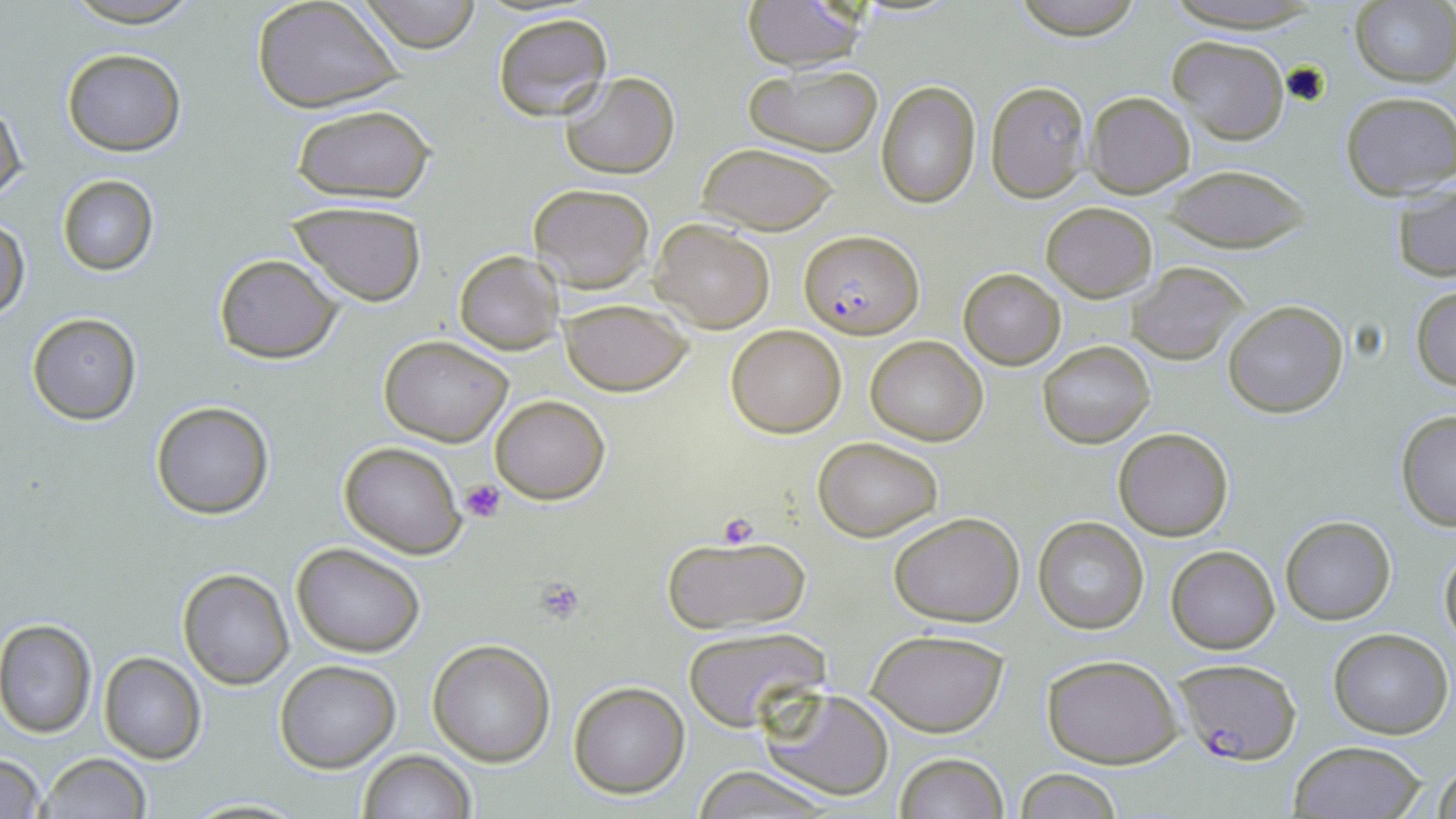

slide_level_diagnosis: Plasmodium falciparum
stain: May-Grünwald-Giemsa
field_of_view: single
preparation: thin blood smear
uninfected_red_blood_cell_locations: 'approximate bounding boxes as [x1, y1, x2, y2] in pixels: [57, 0, 209, 26], [252, 0, 405, 114], [356, 0, 485, 53], [1008, 0, 1147, 41], [1159, 0, 1323, 33], [741, 1, 869, 70], [1351, 3, 1456, 85], [491, 12, 613, 122], [1165, 35, 1290, 147], [61, 49, 186, 156], [744, 64, 884, 157], [559, 71, 679, 179], [876, 81, 981, 209], [987, 82, 1091, 202], [1339, 91, 1455, 201], [1085, 92, 1195, 198], [1, 96, 26, 205], [289, 104, 437, 204], [696, 142, 842, 235], [1162, 164, 1309, 254], [56, 175, 158, 275], [1392, 181, 1456, 282], [526, 182, 656, 294], [286, 202, 427, 306], [1041, 202, 1157, 301], [0, 216, 28, 321], [650, 219, 775, 333], [454, 250, 566, 355], [212, 253, 343, 364], [1127, 263, 1249, 367], [957, 267, 1067, 370], [1410, 287, 1456, 391], [558, 298, 695, 396], [1222, 300, 1349, 418], [27, 313, 141, 424], [725, 324, 847, 438], [378, 334, 513, 445], [866, 335, 988, 446], [1038, 340, 1155, 448], [489, 394, 611, 505], [150, 400, 274, 518], [1396, 409, 1456, 531], [1114, 427, 1234, 541], [813, 435, 944, 542], [338, 440, 465, 559], [887, 511, 1026, 625], [1280, 515, 1397, 624], [1033, 516, 1149, 635], [662, 531, 811, 638], [1439, 540, 1456, 648], [290, 541, 426, 658], [1165, 545, 1281, 654], [178, 568, 293, 689], [0, 619, 97, 737], [682, 625, 829, 730], [1328, 628, 1453, 738], [866, 629, 1009, 737], [428, 639, 555, 767], [98, 651, 206, 764], [1041, 654, 1184, 768], [273, 659, 400, 771], [568, 681, 690, 799], [758, 686, 893, 802], [1288, 740, 1426, 819], [357, 749, 476, 819], [892, 752, 1009, 819], [38, 753, 150, 819], [0, 754, 46, 819], [1429, 754, 1456, 818], [688, 768, 840, 818], [1013, 768, 1123, 819]'
platelet_locations: 'approximate bounding boxes as [x1, y1, x2, y2] in pixels: [460, 479, 506, 523], [714, 513, 765, 550], [534, 580, 588, 626]'
image_size: 1456×819 pixels
magnification: 1000x
plasmodium_falciparum_infected_red_blood_cell_locations: 'approximate bounding boxes as [x1, y1, x2, y2] in pixels: [799, 229, 923, 339], [1170, 656, 1300, 763]'
modality: light microscopy